Find the red blood cells that are infected with P. falciparum, and any of indeterminate infection status.
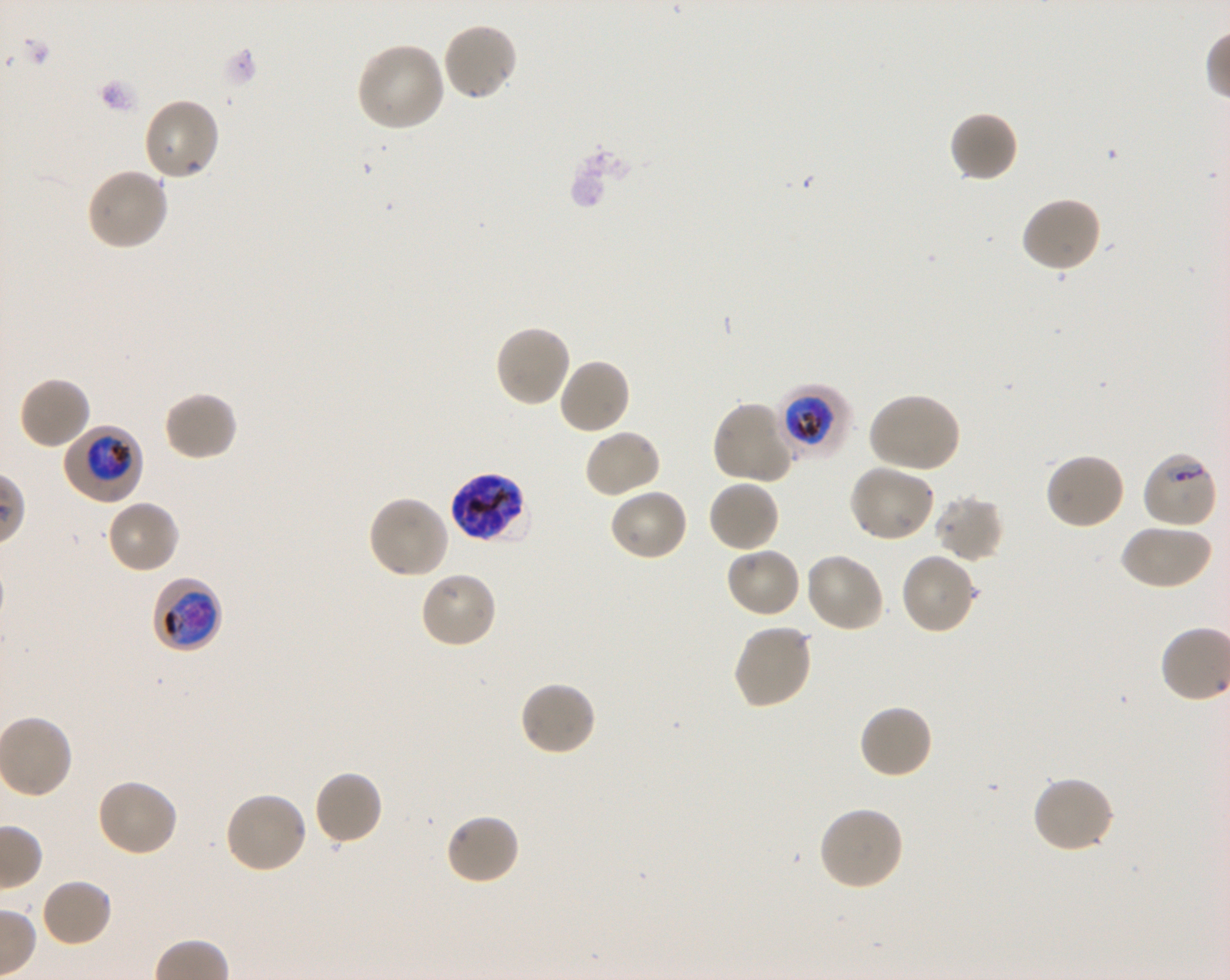

Approximate bounding boxes as (x1, y1, x2, y2) in pixels. Not every red blood cell is marked. A life-cycle stage — or a range of stages, where the recorded stages span more than one — follows each staged infected red blood cell.
Infected red blood cells: (778, 385, 850, 461) trophozoite; (63, 425, 143, 503) trophozoite; (450, 472, 528, 544) schizont; (151, 575, 222, 654) trophozoite.
Red blood cells of indeterminate infection status: (1142, 451, 1218, 530).

Locations of uninfected red blood cells: (441, 22, 519, 103), (355, 41, 447, 131), (142, 97, 220, 182), (950, 112, 1019, 184), (85, 167, 170, 251), (1019, 196, 1103, 275), (494, 325, 573, 408), (556, 357, 631, 435), (17, 376, 92, 451), (163, 390, 239, 462), (868, 392, 962, 474), (713, 401, 795, 485), (582, 429, 662, 499), (1044, 452, 1126, 531), (847, 465, 935, 543), (706, 479, 780, 553), (608, 487, 690, 562), (366, 495, 449, 580), (933, 495, 1004, 563), (105, 498, 180, 574), (1119, 523, 1212, 590), (724, 546, 802, 619), (804, 552, 886, 632), (900, 552, 977, 634), (419, 571, 497, 650), (732, 623, 813, 710), (518, 680, 598, 757), (858, 703, 934, 780), (312, 769, 384, 847), (1032, 775, 1115, 855), (95, 778, 179, 858), (224, 790, 309, 874), (817, 805, 905, 891), (444, 812, 521, 886), (38, 877, 113, 948). Life-cycle stages observed: trophozoite, schizont. Giemsa-stained preparation. Thin blood smear. Oil immersion, 100x objective (numerical aperture 1.30). Image is 1230×980 pixels. P. falciparum strain 3D7 in shaking in-vitro culture. One field from this slide. Blood group of the donor: O+.